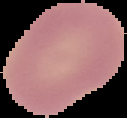
Summary:
  - Image type: cell region segmented out of the field of view; surrounding area masked to black
  - Malaria status: uninfected
  - Preparation: thin blood smear
  - Image size: 127×118 pixels